Comment on the morphology of the red blood cells.
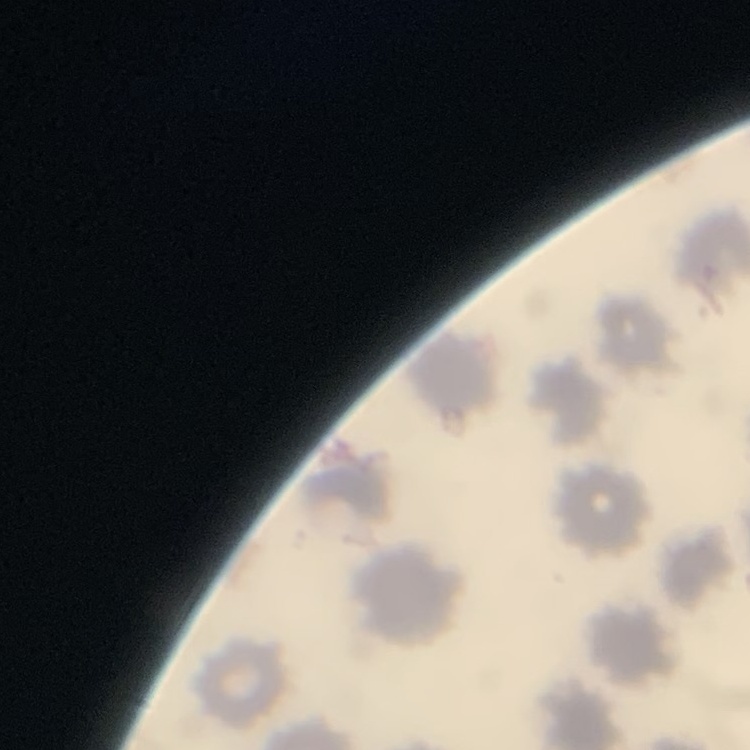

They show no rouleaux formation.

Summary:
  - Stain: Field's or Giemsa
  - Image type: square crop of a larger photomicrograph
  - Preparation: thin blood film